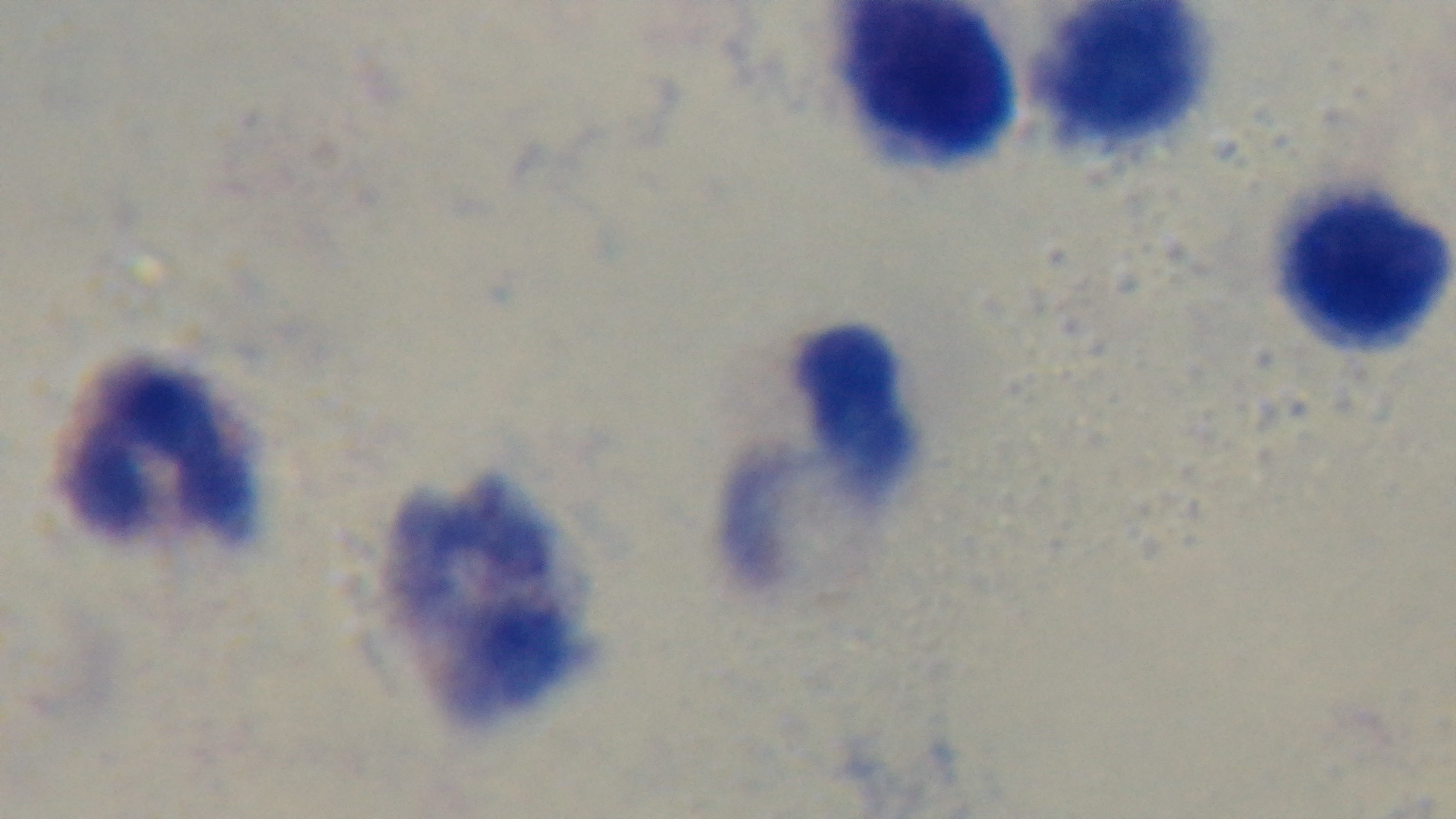

Summary:
  - Modality: light microscopy
  - Preparation: thick smear
  - Malaria status: uninfected
  - Capture: mounted 4K digital camera
  - Field of view: one from the slide
  - Stain: Giemsa
  - Objective: 100x oil immersion